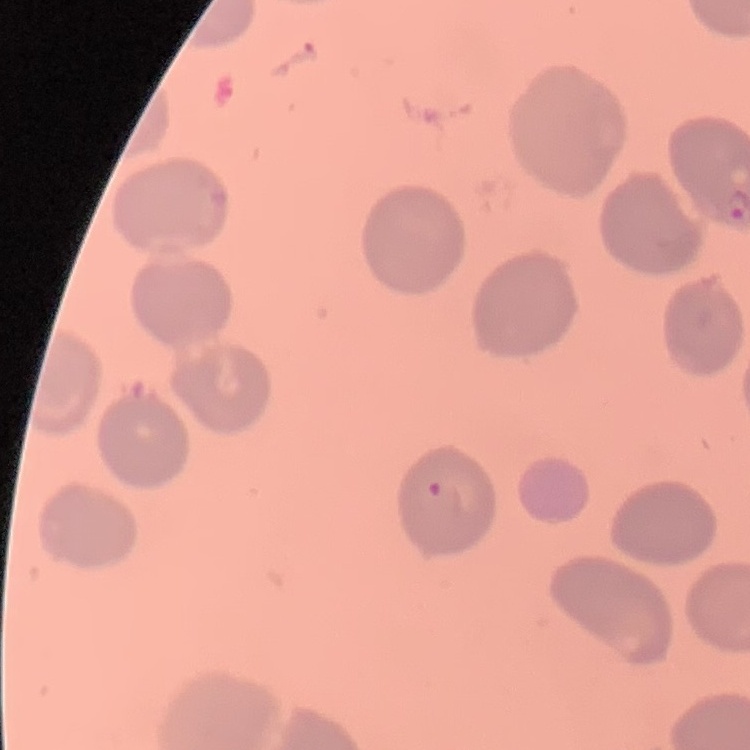

Summary:
  - Erythrocyte morphology: no rouleaux formation
  - Stain: Field's or Giemsa
  - Image type: one tile cut from a larger photomicrograph
  - Preparation: thin blood film